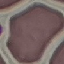

{
  "malaria_status": "uninfected",
  "image_type": "cell patch, automatically extracted from a larger field of view and resized to 64 × 64 pixels",
  "stain": "Giemsa",
  "preparation": "thin blood smear",
  "capture": "smartphone through the microscope eyepiece"
}